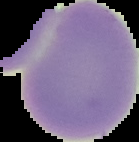

preparation = thin blood smear
image type = cell region segmented out of the field of view; surrounding area masked to black
image size = 139×142 pixels
malaria status = uninfected